Identify the blood parasite species.
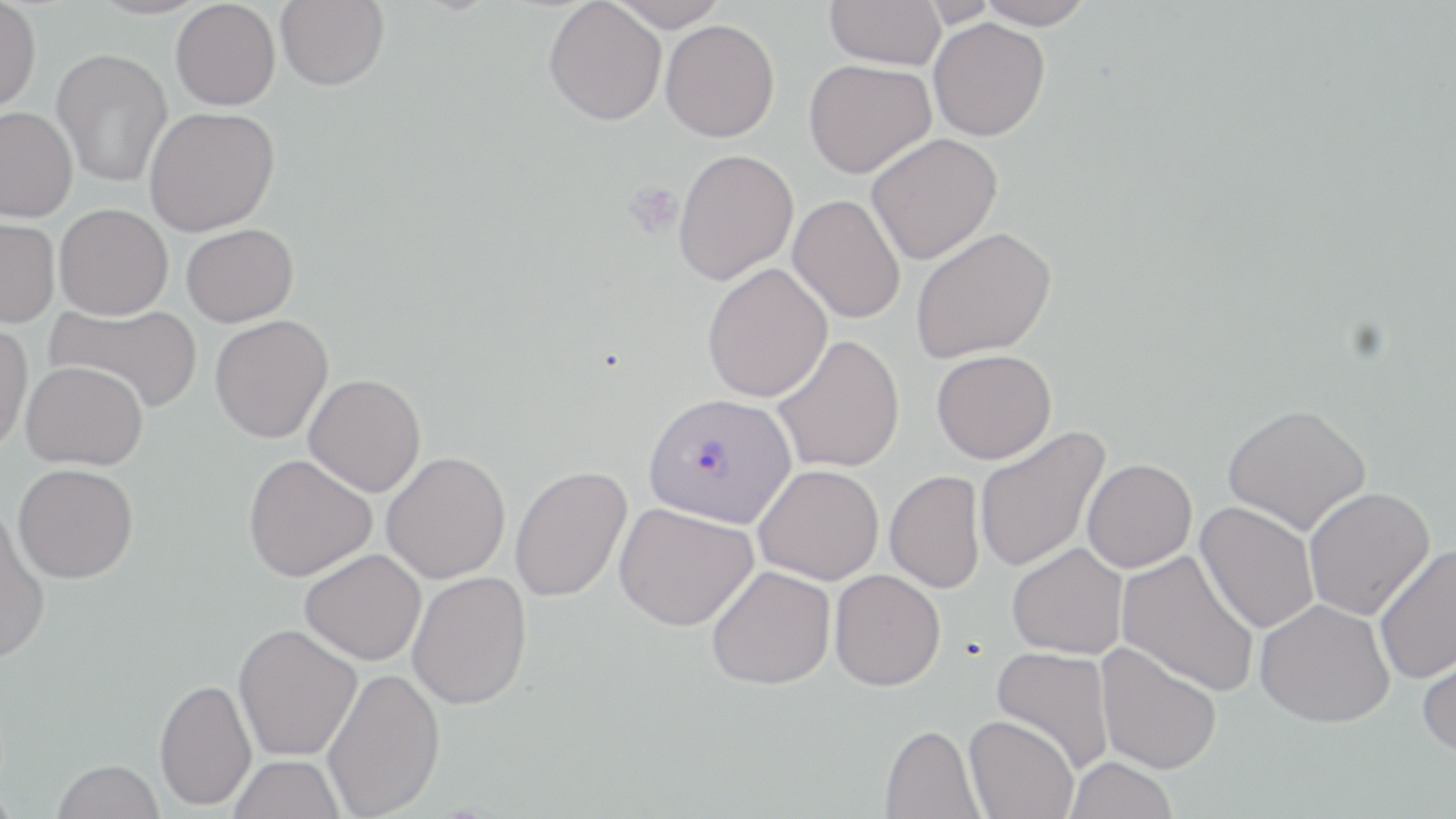
Plasmodium vivax.

Approximate bounding boxes as named x1/y1/x2/y2 corners in pixels. Platelet locations: (x1=623, y1=181, x2=684, y2=237). Uninfected red blood cell locations: (x1=275, y1=0, x2=389, y2=90), (x1=606, y1=0, x2=730, y2=31), (x1=825, y1=0, x2=946, y2=69), (x1=974, y1=0, x2=1096, y2=29), (x1=171, y1=1, x2=280, y2=111), (x1=543, y1=1, x2=667, y2=125), (x1=0, y1=2, x2=41, y2=114), (x1=928, y1=19, x2=1050, y2=141), (x1=660, y1=20, x2=780, y2=142), (x1=52, y1=48, x2=172, y2=187), (x1=803, y1=59, x2=935, y2=178), (x1=0, y1=106, x2=78, y2=223), (x1=144, y1=106, x2=279, y2=236), (x1=866, y1=133, x2=1003, y2=264), (x1=673, y1=148, x2=798, y2=285), (x1=788, y1=194, x2=906, y2=324), (x1=55, y1=203, x2=173, y2=319), (x1=0, y1=217, x2=59, y2=328), (x1=181, y1=224, x2=299, y2=327), (x1=910, y1=227, x2=1056, y2=363), (x1=702, y1=264, x2=833, y2=402), (x1=47, y1=302, x2=203, y2=413), (x1=210, y1=314, x2=333, y2=443), (x1=0, y1=320, x2=33, y2=455), (x1=772, y1=334, x2=905, y2=473), (x1=932, y1=349, x2=1057, y2=463), (x1=22, y1=361, x2=148, y2=470), (x1=304, y1=374, x2=426, y2=497), (x1=1222, y1=403, x2=1371, y2=536), (x1=974, y1=426, x2=1110, y2=574), (x1=381, y1=451, x2=510, y2=584), (x1=243, y1=454, x2=376, y2=581), (x1=1082, y1=458, x2=1197, y2=573), (x1=12, y1=463, x2=139, y2=583), (x1=754, y1=464, x2=884, y2=584), (x1=509, y1=465, x2=633, y2=603), (x1=884, y1=470, x2=985, y2=594), (x1=1303, y1=487, x2=1435, y2=620), (x1=1195, y1=501, x2=1319, y2=634), (x1=614, y1=502, x2=759, y2=631), (x1=0, y1=509, x2=51, y2=664), (x1=1006, y1=542, x2=1128, y2=660), (x1=1373, y1=542, x2=1456, y2=685), (x1=300, y1=548, x2=426, y2=665), (x1=1117, y1=549, x2=1261, y2=697), (x1=707, y1=565, x2=836, y2=690), (x1=829, y1=569, x2=945, y2=691), (x1=407, y1=571, x2=532, y2=710), (x1=1255, y1=599, x2=1394, y2=728), (x1=233, y1=623, x2=362, y2=761), (x1=1416, y1=637, x2=1456, y2=760), (x1=1095, y1=642, x2=1222, y2=774), (x1=991, y1=646, x2=1116, y2=773), (x1=322, y1=667, x2=445, y2=817), (x1=154, y1=677, x2=257, y2=810), (x1=963, y1=715, x2=1078, y2=819), (x1=880, y1=724, x2=983, y2=819), (x1=228, y1=754, x2=346, y2=819), (x1=1064, y1=757, x2=1178, y2=818), (x1=52, y1=759, x2=164, y2=819). Plasmodium vivax-infected red blood cell locations: (x1=643, y1=392, x2=796, y2=527). Captured at 1000x magnification. Thin blood film. Optical microscopy. May-Grünwald-Giemsa-stained preparation. Image is 1456×819 pixels. Single field of view.